Name the cell type shown.
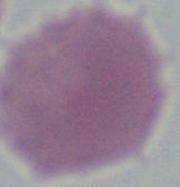
An erythrocyte.

1000x magnification. Photomicrograph.